Report the malaria status of this cell.
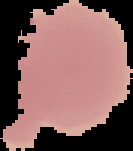
Uninfected.

preparation = thin blood smear
image type = segmented cell region with the area outside set to black
image size = 133×151 pixels